Name the parasite shown.
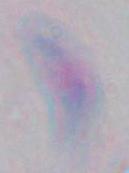
Toxoplasma gondii.

Summary:
  - Magnification: 1000x
  - Modality: photomicrograph